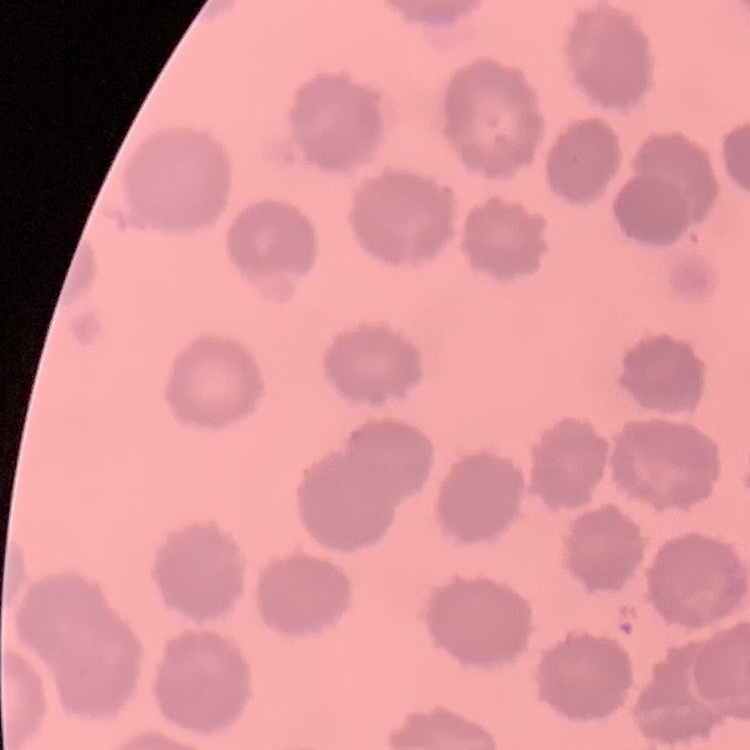
red blood cell morphology = no rouleaux formation
preparation = thin blood smear
image type = square crop of a larger photomicrograph
stain = Field's or Giemsa